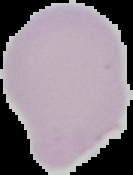
Image is 133×175 pixels. Cell region segmented out of the field of view; the surrounding area is masked to black. Result: no malaria parasites seen. From a thin blood smear.